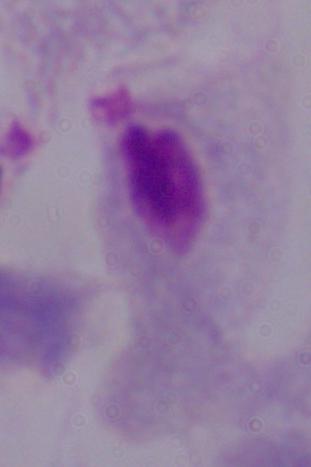

Summary:
  - Modality: photomicrograph
  - Identification: trichomonad
  - Magnification: 1000x